Give the position of every P. falciparum parasite, noting its life-cycle stage.
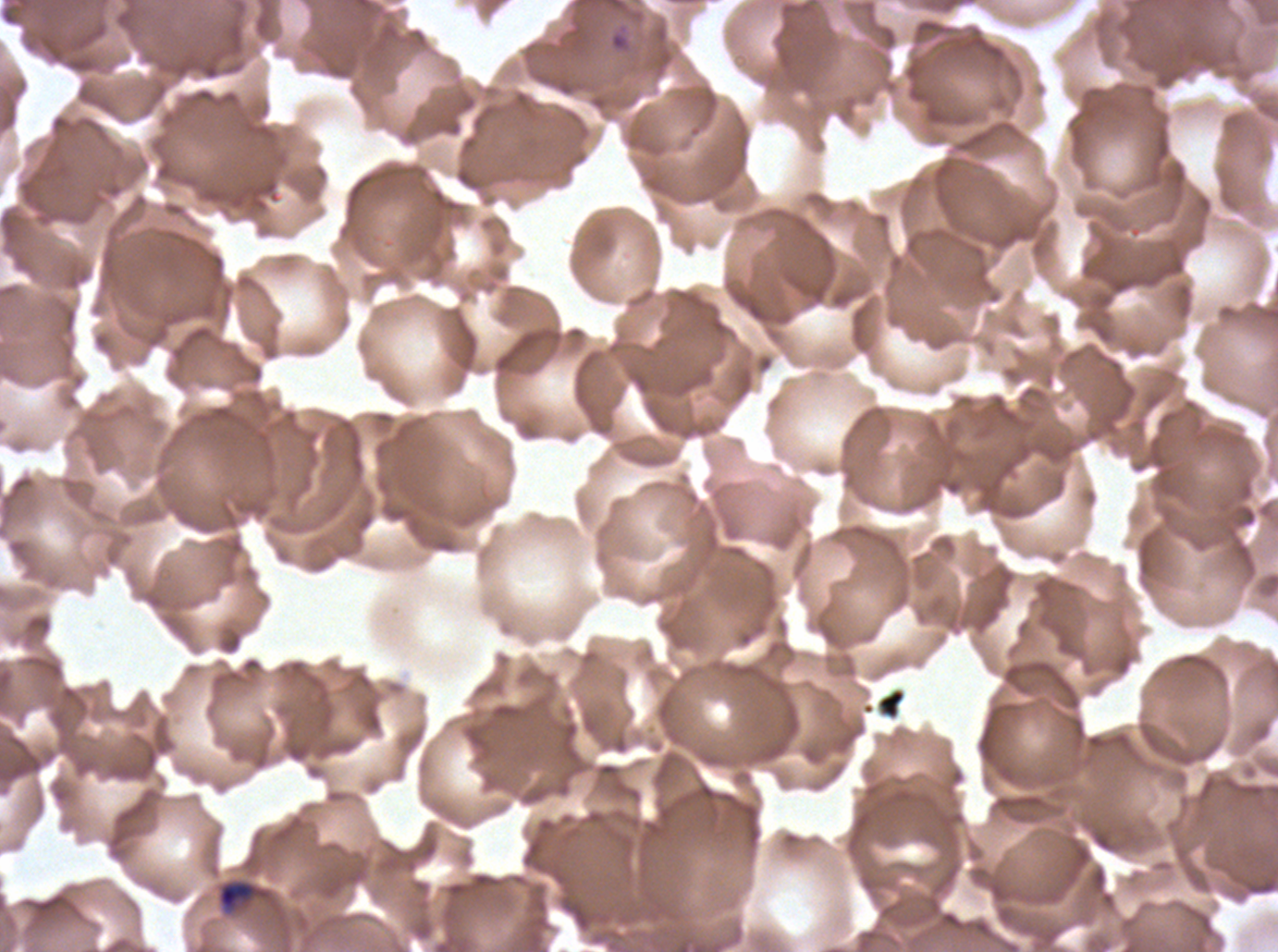

Approximate bounding boxes as {x1, y1, x2, y2} in pixels.
Rings: {608, 30, 631, 53}.
Late-ring/early-trophozoite forms: {216, 879, 259, 912}.
No mid trophozoites, late trophozoites, early schizonts, late schizonts, segmenters, or gametocytes observed.

Debris locations: {876, 687, 906, 720}. Thin blood smear. Giemsa stain. Image is 1278×952 pixels. Life-cycle stages observed: ring, late-ring/early-trophozoite. One sub-image of a larger composite. P. falciparum from a patient in The Gambia, cultured ex vivo for 24 to 48 hours.